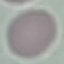
Summary:
  - Result: negative for malaria parasites
  - Stain: Giemsa
  - Image type: automatically extracted cell patch, resized to 64 × 64 pixels
  - Capture: smartphone through the microscope eyepiece
  - Preparation: thin blood smear